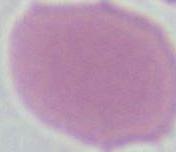
Summary:
  - Modality: micrograph
  - Identification: erythrocyte
  - Magnification: 1000x